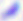
identification = Toxoplasma gondii
modality = micrograph
magnification = 400x